Report the malaria status of this cell.
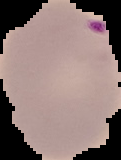
Parasitized.

image size = 121×160 pixels
preparation = thin blood film
image type = cell region segmented out of the field of view; surrounding area masked to black